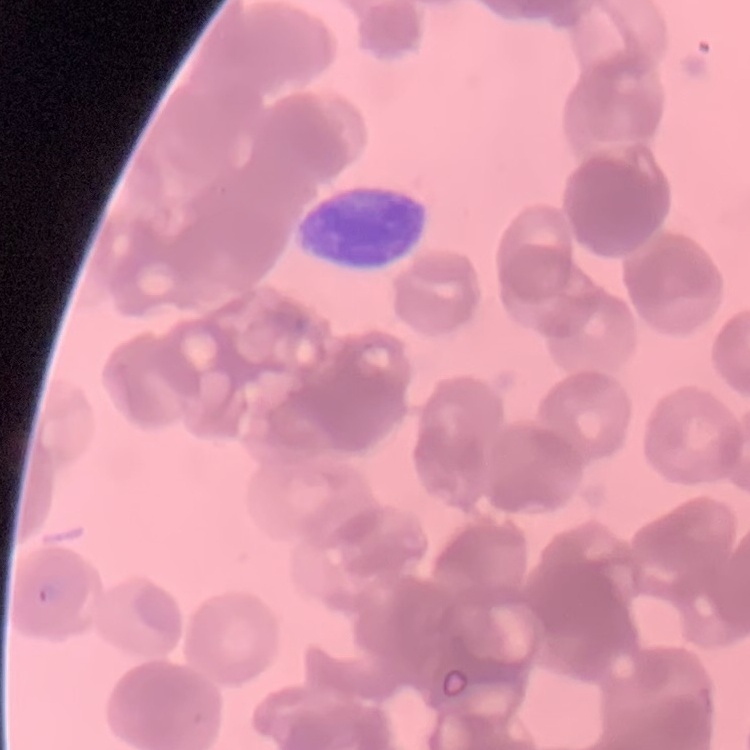
The erythrocytes exhibit rouleaux formation. Stained with either Field's or Giemsa. Thin blood smear. One tile cut from a larger photomicrograph.